State which parasite is depicted.
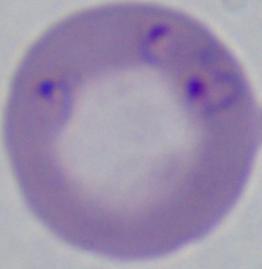

This is Babesia.

Micrograph. 1000x magnification.